Outline each blood parasite and name the species.
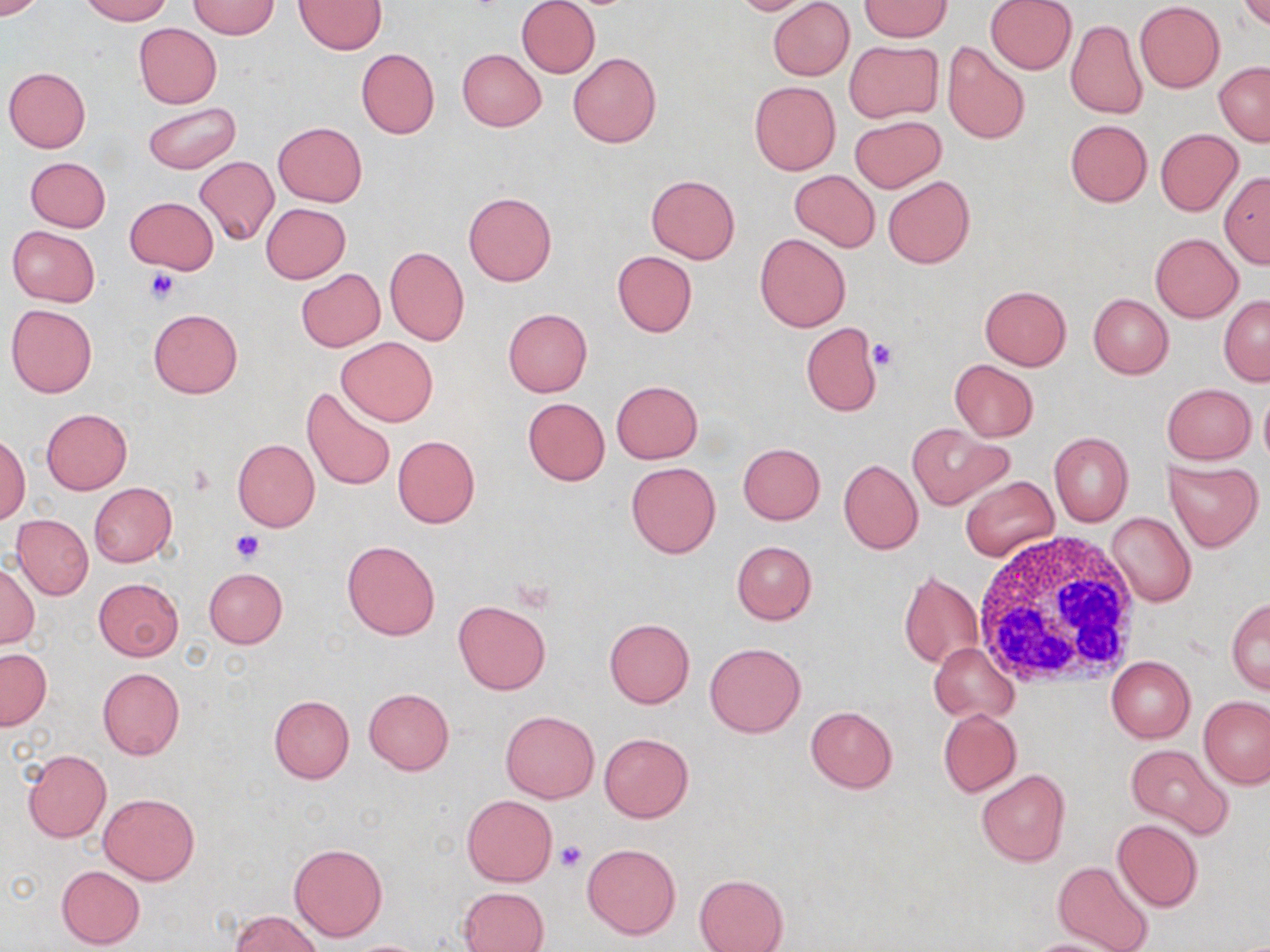

No blood parasites seen.

Summary:
  - Coordinate format: approximate bounding boxes as named x1/y1/x2/y2 corners in pixels
  - Uninfected red blood cell locations: (x1=0, y1=0, x2=47, y2=19), (x1=81, y1=0, x2=170, y2=24), (x1=295, y1=0, x2=386, y2=54), (x1=517, y1=0, x2=600, y2=79), (x1=726, y1=0, x2=820, y2=15), (x1=767, y1=0, x2=854, y2=81), (x1=984, y1=0, x2=1076, y2=74), (x1=1238, y1=0, x2=1269, y2=31), (x1=187, y1=1, x2=280, y2=39), (x1=1135, y1=1, x2=1225, y2=92), (x1=860, y1=2, x2=952, y2=41), (x1=1066, y1=19, x2=1147, y2=119), (x1=134, y1=23, x2=222, y2=107), (x1=941, y1=40, x2=1031, y2=145), (x1=845, y1=41, x2=942, y2=123), (x1=356, y1=49, x2=440, y2=138), (x1=457, y1=49, x2=547, y2=131), (x1=567, y1=51, x2=662, y2=148), (x1=1214, y1=62, x2=1270, y2=146), (x1=3, y1=67, x2=91, y2=152), (x1=749, y1=82, x2=840, y2=175), (x1=144, y1=101, x2=240, y2=173), (x1=849, y1=115, x2=945, y2=192), (x1=1065, y1=120, x2=1152, y2=206), (x1=274, y1=122, x2=367, y2=207), (x1=1155, y1=128, x2=1243, y2=216), (x1=195, y1=155, x2=279, y2=246), (x1=25, y1=157, x2=110, y2=232), (x1=790, y1=169, x2=880, y2=251), (x1=1219, y1=171, x2=1270, y2=268), (x1=645, y1=174, x2=741, y2=263), (x1=882, y1=176, x2=975, y2=268), (x1=463, y1=192, x2=556, y2=286), (x1=125, y1=197, x2=218, y2=274), (x1=260, y1=203, x2=350, y2=284), (x1=6, y1=225, x2=99, y2=307), (x1=754, y1=233, x2=851, y2=333), (x1=1150, y1=233, x2=1242, y2=322), (x1=384, y1=246, x2=470, y2=346), (x1=611, y1=250, x2=697, y2=336), (x1=295, y1=269, x2=385, y2=351), (x1=979, y1=285, x2=1072, y2=370), (x1=1088, y1=294, x2=1172, y2=379), (x1=1218, y1=295, x2=1270, y2=385), (x1=6, y1=303, x2=97, y2=397), (x1=148, y1=308, x2=242, y2=398), (x1=503, y1=308, x2=592, y2=397), (x1=801, y1=322, x2=881, y2=417), (x1=336, y1=338, x2=439, y2=427), (x1=949, y1=359, x2=1038, y2=441), (x1=610, y1=380, x2=703, y2=463), (x1=1163, y1=384, x2=1255, y2=464), (x1=1259, y1=386, x2=1270, y2=469), (x1=302, y1=387, x2=396, y2=493), (x1=522, y1=398, x2=610, y2=486), (x1=41, y1=408, x2=132, y2=493), (x1=907, y1=423, x2=1010, y2=510), (x1=1049, y1=432, x2=1133, y2=526), (x1=392, y1=434, x2=480, y2=527), (x1=0, y1=436, x2=29, y2=524), (x1=232, y1=438, x2=320, y2=532), (x1=737, y1=442, x2=825, y2=524), (x1=838, y1=460, x2=923, y2=554), (x1=1165, y1=460, x2=1263, y2=550), (x1=625, y1=462, x2=721, y2=559), (x1=960, y1=476, x2=1058, y2=561), (x1=89, y1=483, x2=177, y2=567), (x1=1106, y1=512, x2=1196, y2=608), (x1=12, y1=514, x2=93, y2=601), (x1=341, y1=540, x2=440, y2=640), (x1=731, y1=541, x2=817, y2=625), (x1=0, y1=560, x2=40, y2=649), (x1=204, y1=567, x2=287, y2=648), (x1=898, y1=570, x2=983, y2=670), (x1=94, y1=578, x2=184, y2=660), (x1=1227, y1=598, x2=1270, y2=694), (x1=454, y1=600, x2=552, y2=694), (x1=604, y1=619, x2=695, y2=708), (x1=704, y1=642, x2=806, y2=738), (x1=928, y1=643, x2=1018, y2=724), (x1=1, y1=648, x2=52, y2=730), (x1=1106, y1=657, x2=1195, y2=743), (x1=97, y1=667, x2=185, y2=759), (x1=363, y1=688, x2=455, y2=774), (x1=268, y1=695, x2=354, y2=783), (x1=1200, y1=696, x2=1270, y2=788), (x1=806, y1=706, x2=897, y2=792), (x1=938, y1=709, x2=1020, y2=796), (x1=500, y1=711, x2=598, y2=803), (x1=599, y1=733, x2=694, y2=823), (x1=1124, y1=744, x2=1234, y2=840), (x1=22, y1=749, x2=110, y2=843), (x1=976, y1=769, x2=1071, y2=867), (x1=99, y1=793, x2=199, y2=884), (x1=463, y1=795, x2=557, y2=885), (x1=1112, y1=819, x2=1203, y2=913), (x1=289, y1=842, x2=387, y2=942), (x1=582, y1=843, x2=681, y2=939), (x1=1053, y1=861, x2=1156, y2=952), (x1=56, y1=865, x2=144, y2=949), (x1=694, y1=874, x2=788, y2=952), (x1=457, y1=886, x2=550, y2=952), (x1=230, y1=911, x2=325, y2=952), (x1=1022, y1=938, x2=1127, y2=952)
  - White blood cell locations: (x1=969, y1=528, x2=1141, y2=691)
  - Platelet locations: (x1=145, y1=267, x2=179, y2=305), (x1=867, y1=338, x2=898, y2=370), (x1=232, y1=529, x2=265, y2=563), (x1=553, y1=837, x2=587, y2=872)
  - Slide-level diagnosis: negative for blood parasites
  - Modality: optical microscopy
  - Image size: 1270×952 pixels
  - Preparation: thin blood smear
  - Stain: May-Grünwald-Giemsa
  - Field of view: single
  - Magnification: 1000x